Name the parasite shown.
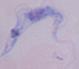
This is a trypanosome.

Captured at 1000x magnification. Micrograph.